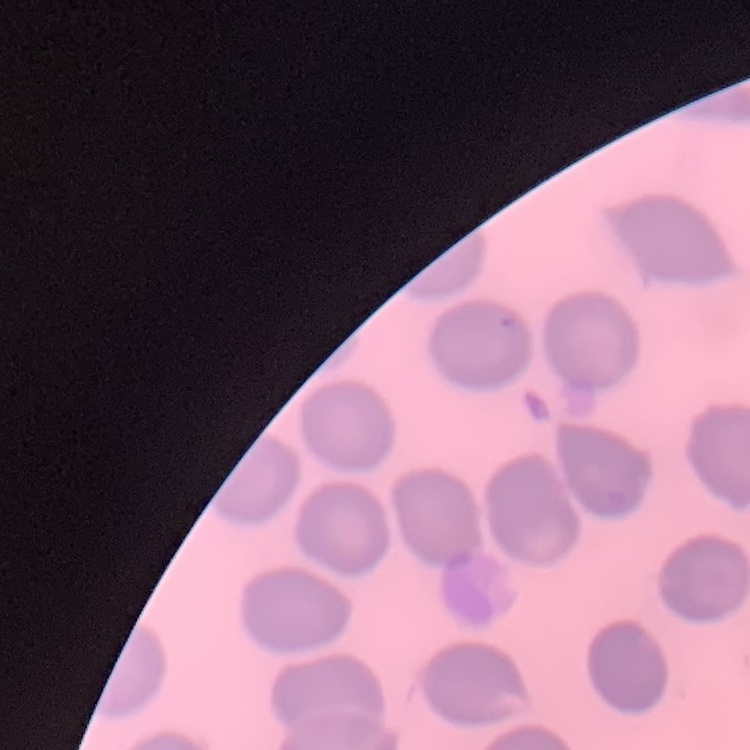
red blood cell morphology = no rouleaux formation
preparation = thin blood smear
stain = Field's or Giemsa
image type = one tile cut from a larger photomicrograph